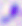

Summary:
  - Modality: micrograph
  - Magnification: 400x
  - Identification: Toxoplasma gondii